State the blood parasite species.
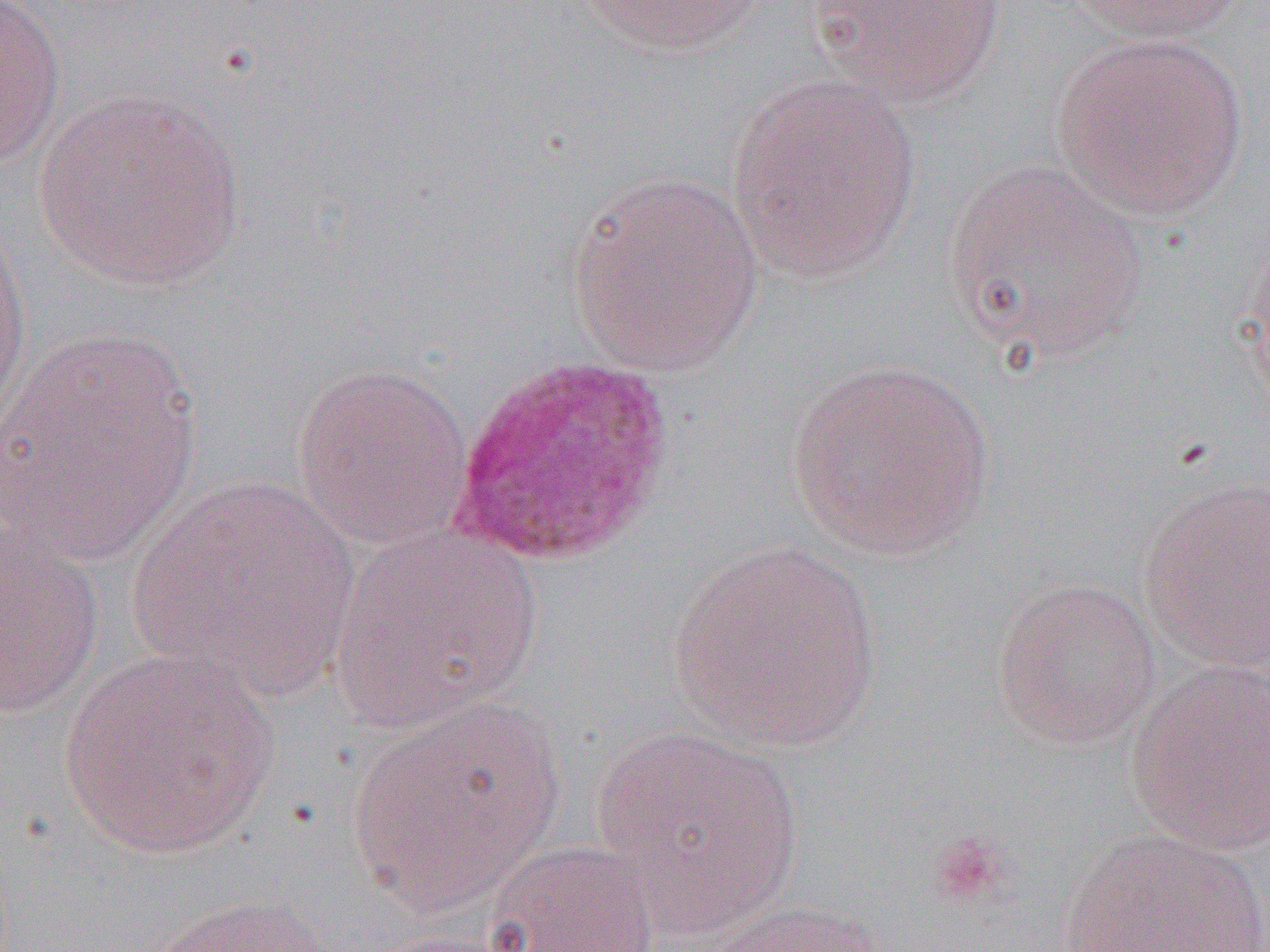

Plasmodium ovale.

Summary:
  - Coordinate format: approximate bounding boxes as named x1/y1/x2/y2 corners in pixels
  - Uninfected red blood cell locations: (x1=575, y1=0, x2=771, y2=58), (x1=804, y1=0, x2=1007, y2=108), (x1=1067, y1=0, x2=1251, y2=45), (x1=0, y1=1, x2=68, y2=172), (x1=1050, y1=33, x2=1249, y2=221), (x1=726, y1=76, x2=923, y2=284), (x1=33, y1=89, x2=246, y2=291), (x1=941, y1=160, x2=1150, y2=362), (x1=564, y1=171, x2=764, y2=376), (x1=0, y1=219, x2=33, y2=429), (x1=1243, y1=234, x2=1270, y2=418), (x1=3, y1=325, x2=203, y2=567), (x1=787, y1=357, x2=997, y2=559), (x1=292, y1=361, x2=475, y2=553), (x1=128, y1=474, x2=362, y2=701), (x1=1136, y1=475, x2=1269, y2=676), (x1=0, y1=524, x2=105, y2=721), (x1=329, y1=524, x2=544, y2=732), (x1=669, y1=540, x2=883, y2=753), (x1=993, y1=577, x2=1163, y2=749), (x1=60, y1=649, x2=280, y2=859), (x1=1126, y1=660, x2=1269, y2=855), (x1=345, y1=695, x2=566, y2=913), (x1=588, y1=724, x2=809, y2=937), (x1=1055, y1=829, x2=1270, y2=951), (x1=485, y1=841, x2=661, y2=952), (x1=145, y1=893, x2=337, y2=952), (x1=708, y1=900, x2=895, y2=952), (x1=368, y1=927, x2=538, y2=952)
  - Plasmodium ovale-infected red blood cell locations: (x1=450, y1=354, x2=676, y2=567)
  - Platelet locations: (x1=927, y1=830, x2=1010, y2=909)
  - Preparation: thin blood film
  - Field of view: one of a larger specimen
  - Modality: optical microscopy
  - Magnification: 1000x
  - Image size: 1270×952 pixels